Classify this cell by malaria status.
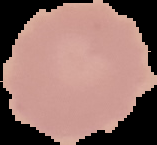

Uninfected.

{
  "image_type": "cell region segmented out of the field of view; surrounding area masked to black",
  "preparation": "thin blood smear",
  "image_size": "157×145 pixels"
}